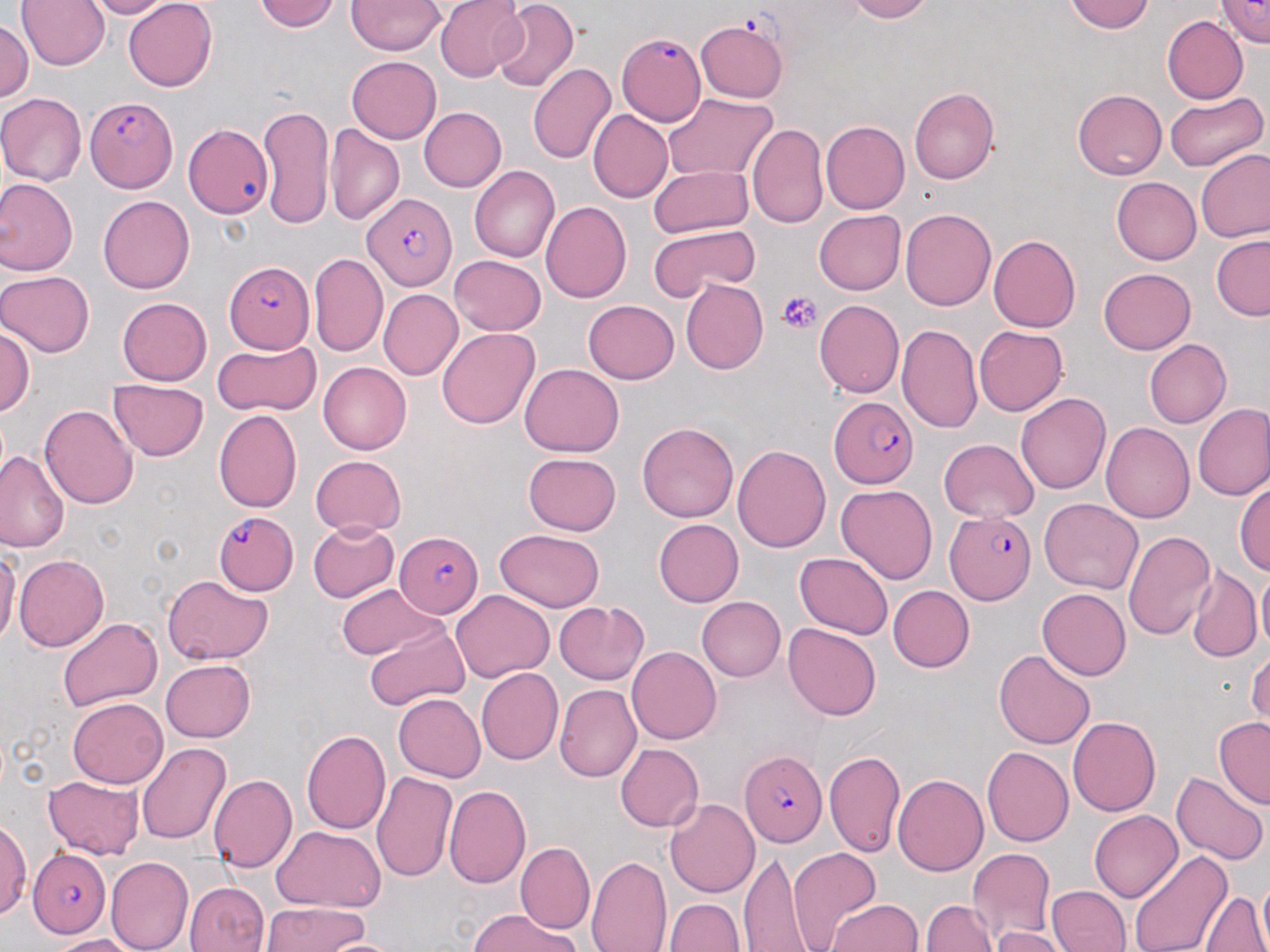

Summary:
  - Coordinate format: approximate bounding boxes as named x1/y1/x2/y2 corners in pixels
  - Plasmodium falciparum-infected red blood cell locations: (x1=615, y1=31, x2=704, y2=126), (x1=85, y1=95, x2=178, y2=193), (x1=362, y1=191, x2=457, y2=287), (x1=223, y1=261, x2=312, y2=354), (x1=827, y1=396, x2=919, y2=487), (x1=216, y1=511, x2=297, y2=593), (x1=943, y1=511, x2=1036, y2=605), (x1=393, y1=531, x2=482, y2=617), (x1=740, y1=752, x2=827, y2=848), (x1=27, y1=850, x2=112, y2=938)
  - Platelet locations: (x1=778, y1=291, x2=823, y2=334)
  - Uninfected red blood cell locations: (x1=83, y1=0, x2=175, y2=18), (x1=121, y1=0, x2=217, y2=92), (x1=253, y1=0, x2=338, y2=34), (x1=347, y1=0, x2=445, y2=56), (x1=436, y1=0, x2=530, y2=78), (x1=839, y1=0, x2=934, y2=23), (x1=1065, y1=0, x2=1156, y2=34), (x1=1218, y1=0, x2=1269, y2=47), (x1=18, y1=1, x2=109, y2=70), (x1=488, y1=2, x2=579, y2=92), (x1=1, y1=15, x2=33, y2=107), (x1=1161, y1=16, x2=1248, y2=104), (x1=695, y1=19, x2=790, y2=102), (x1=346, y1=55, x2=441, y2=143), (x1=528, y1=61, x2=615, y2=164), (x1=910, y1=86, x2=1000, y2=182), (x1=1073, y1=89, x2=1165, y2=179), (x1=0, y1=92, x2=86, y2=185), (x1=1163, y1=92, x2=1266, y2=171), (x1=665, y1=95, x2=779, y2=181), (x1=257, y1=102, x2=338, y2=230), (x1=421, y1=105, x2=507, y2=192), (x1=587, y1=109, x2=673, y2=203), (x1=747, y1=121, x2=829, y2=228), (x1=820, y1=121, x2=910, y2=214), (x1=183, y1=122, x2=276, y2=219), (x1=324, y1=124, x2=405, y2=227), (x1=1196, y1=149, x2=1270, y2=245), (x1=469, y1=166, x2=559, y2=263), (x1=648, y1=166, x2=755, y2=237), (x1=1111, y1=177, x2=1201, y2=265), (x1=0, y1=179, x2=79, y2=274), (x1=97, y1=193, x2=196, y2=293), (x1=541, y1=202, x2=631, y2=302), (x1=899, y1=207, x2=998, y2=310), (x1=814, y1=210, x2=906, y2=295), (x1=648, y1=225, x2=759, y2=302), (x1=988, y1=235, x2=1082, y2=332), (x1=1212, y1=235, x2=1270, y2=321), (x1=311, y1=252, x2=386, y2=356), (x1=450, y1=255, x2=547, y2=334), (x1=1098, y1=267, x2=1195, y2=354), (x1=0, y1=269, x2=94, y2=358), (x1=680, y1=279, x2=769, y2=374), (x1=377, y1=289, x2=461, y2=379), (x1=118, y1=297, x2=211, y2=385), (x1=816, y1=298, x2=904, y2=399), (x1=581, y1=300, x2=678, y2=383), (x1=0, y1=321, x2=34, y2=421), (x1=897, y1=322, x2=982, y2=433), (x1=974, y1=325, x2=1067, y2=415), (x1=437, y1=327, x2=538, y2=431), (x1=212, y1=339, x2=322, y2=416), (x1=1145, y1=339, x2=1232, y2=427), (x1=319, y1=362, x2=412, y2=453), (x1=518, y1=363, x2=624, y2=458), (x1=109, y1=377, x2=210, y2=460), (x1=1017, y1=391, x2=1111, y2=497), (x1=41, y1=404, x2=137, y2=511), (x1=1194, y1=404, x2=1270, y2=503), (x1=214, y1=409, x2=303, y2=512), (x1=637, y1=422, x2=739, y2=523), (x1=1102, y1=424, x2=1194, y2=524), (x1=939, y1=438, x2=1040, y2=523), (x1=734, y1=442, x2=830, y2=554), (x1=2, y1=450, x2=66, y2=552), (x1=311, y1=454, x2=407, y2=535), (x1=522, y1=454, x2=622, y2=535), (x1=1235, y1=477, x2=1270, y2=580), (x1=836, y1=484, x2=938, y2=585), (x1=1039, y1=497, x2=1143, y2=592), (x1=655, y1=518, x2=747, y2=606), (x1=308, y1=521, x2=398, y2=603), (x1=493, y1=527, x2=606, y2=611), (x1=1123, y1=528, x2=1217, y2=644), (x1=0, y1=540, x2=18, y2=654), (x1=793, y1=550, x2=894, y2=639), (x1=13, y1=552, x2=108, y2=650), (x1=1186, y1=566, x2=1258, y2=661), (x1=1256, y1=567, x2=1270, y2=657), (x1=160, y1=575, x2=274, y2=664), (x1=339, y1=583, x2=441, y2=661), (x1=887, y1=584, x2=972, y2=672), (x1=451, y1=588, x2=552, y2=680), (x1=1038, y1=588, x2=1130, y2=680), (x1=697, y1=597, x2=785, y2=681), (x1=557, y1=600, x2=650, y2=683), (x1=58, y1=616, x2=162, y2=713), (x1=359, y1=617, x2=471, y2=716), (x1=783, y1=622, x2=883, y2=721), (x1=1250, y1=645, x2=1270, y2=727), (x1=627, y1=646, x2=721, y2=745), (x1=994, y1=647, x2=1094, y2=746), (x1=161, y1=660, x2=257, y2=742), (x1=477, y1=668, x2=562, y2=764), (x1=555, y1=683, x2=639, y2=780), (x1=392, y1=693, x2=485, y2=782), (x1=68, y1=698, x2=167, y2=788), (x1=1068, y1=716, x2=1162, y2=815), (x1=1213, y1=719, x2=1269, y2=807), (x1=300, y1=728, x2=392, y2=835), (x1=136, y1=741, x2=230, y2=845), (x1=614, y1=743, x2=702, y2=833), (x1=982, y1=746, x2=1073, y2=844), (x1=826, y1=747, x2=907, y2=861), (x1=1174, y1=769, x2=1267, y2=866), (x1=372, y1=772, x2=456, y2=883), (x1=893, y1=774, x2=988, y2=874), (x1=42, y1=775, x2=146, y2=859), (x1=207, y1=775, x2=295, y2=873), (x1=444, y1=783, x2=530, y2=890), (x1=666, y1=796, x2=760, y2=897), (x1=1089, y1=809, x2=1183, y2=903), (x1=0, y1=816, x2=31, y2=919), (x1=269, y1=827, x2=384, y2=914), (x1=517, y1=842, x2=594, y2=932), (x1=967, y1=846, x2=1057, y2=945), (x1=788, y1=847, x2=882, y2=952), (x1=1129, y1=850, x2=1232, y2=952), (x1=741, y1=853, x2=814, y2=950), (x1=586, y1=855, x2=672, y2=952), (x1=109, y1=857, x2=190, y2=951), (x1=1251, y1=875, x2=1269, y2=952), (x1=184, y1=878, x2=272, y2=951), (x1=1046, y1=885, x2=1128, y2=952), (x1=1200, y1=887, x2=1268, y2=952), (x1=663, y1=896, x2=746, y2=952), (x1=827, y1=897, x2=923, y2=952), (x1=923, y1=898, x2=999, y2=952), (x1=260, y1=902, x2=375, y2=952), (x1=467, y1=911, x2=579, y2=952), (x1=987, y1=925, x2=1068, y2=952), (x1=45, y1=934, x2=137, y2=951), (x1=326, y1=934, x2=402, y2=952)
  - Slide-level diagnosis: Plasmodium falciparum
  - Stain: May-Grünwald-Giemsa
  - Image size: 1270×952 pixels
  - Preparation: thin blood film
  - Magnification: 1000x
  - Modality: optical microscopy
  - Field of view: single